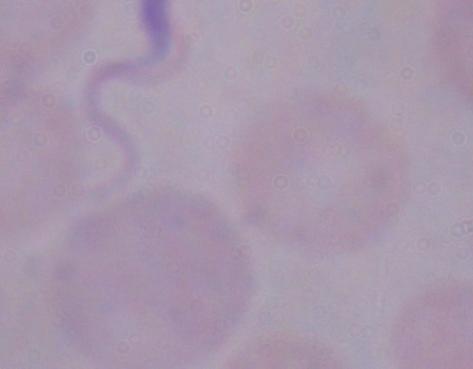

Summary:
  - Modality: micrograph
  - Magnification: 1000x
  - Identification: trypanosome